Assess this cell for malaria.
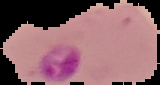
Parasitized.

From a thin blood film. Image is 160×85 pixels. The area outside the segmented cell region is set to black.